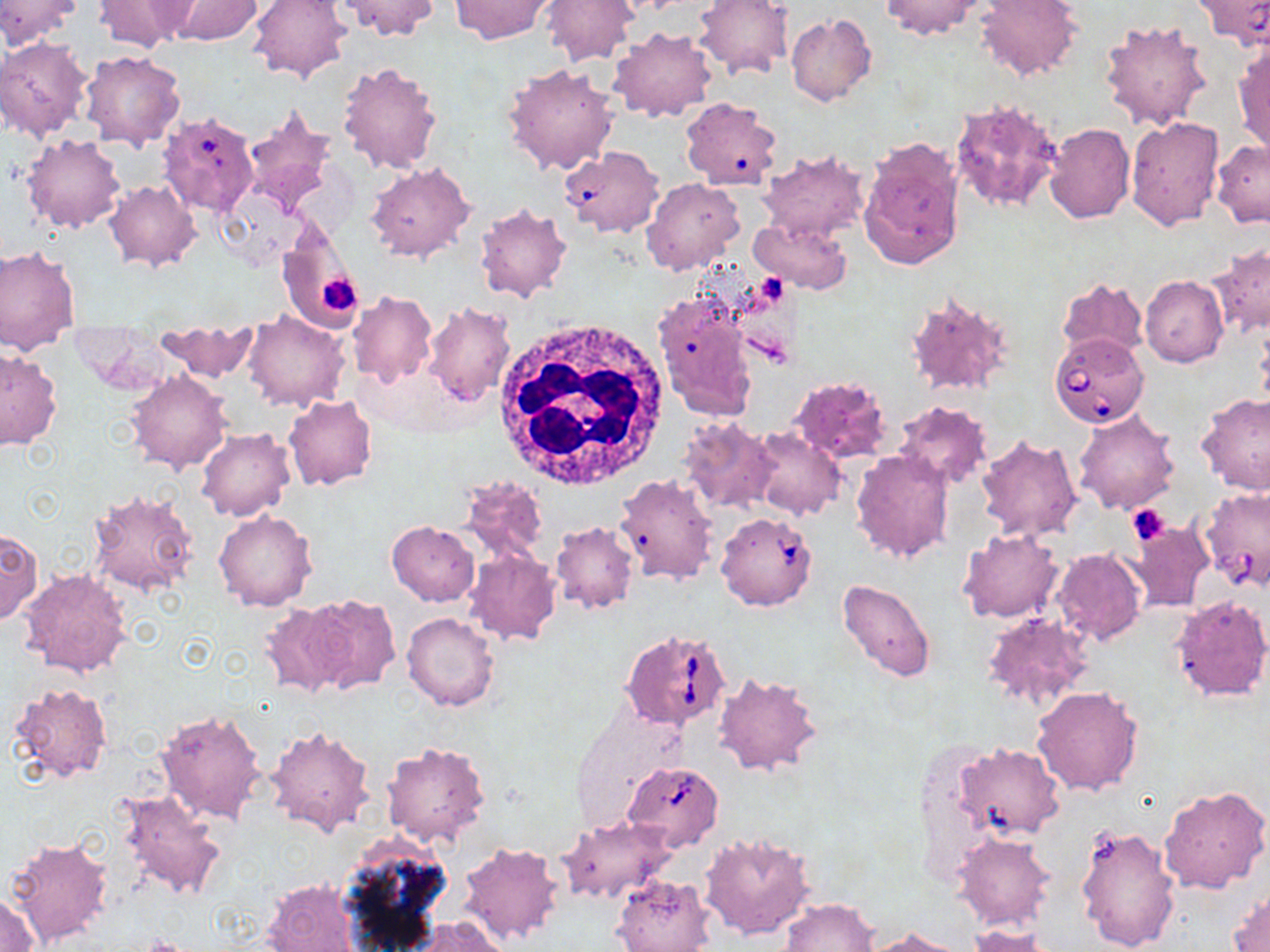
slide-level diagnosis = Babesia divergens
magnification = 1000x
uninfected red blood cell locations = approximate bounding boxes as (x1,y1)-(x2,y2) corner pairs in pixels: (0,0)-(83,48), (92,0)-(197,52), (162,0)-(263,44), (246,0)-(350,83), (334,0)-(440,41), (542,0)-(638,65), (693,0)-(793,79), (879,0)-(985,40), (975,0)-(1081,82), (449,1)-(555,43), (786,14)-(876,106), (1100,18)-(1211,131), (609,27)-(715,123), (0,38)-(91,140), (1233,40)-(1270,157), (81,50)-(186,150), (338,60)-(443,174), (502,63)-(621,175), (949,96)-(1066,213), (681,101)-(782,189), (239,104)-(339,217), (1126,117)-(1225,231), (1044,122)-(1135,223), (20,134)-(124,234), (858,139)-(965,271), (1210,140)-(1270,226), (560,148)-(659,236), (758,148)-(870,242), (366,162)-(475,264), (642,178)-(744,275), (105,181)-(201,271), (473,203)-(572,303), (748,217)-(852,295), (277,226)-(365,333), (1209,243)-(1269,336), (0,246)-(81,345), (1140,275)-(1228,369), (1056,277)-(1149,360), (653,286)-(760,420), (906,290)-(1015,398), (348,291)-(436,389), (423,303)-(515,407), (242,310)-(348,412), (156,324)-(257,384), (0,349)-(62,450), (125,370)-(231,474), (790,374)-(891,463), (1195,392)-(1270,494), (283,396)-(377,490), (893,401)-(993,489), (1073,409)-(1180,514), (676,417)-(780,512), (751,427)-(845,520), (196,428)-(293,521), (976,434)-(1081,541), (851,449)-(955,564), (614,474)-(719,585), (456,476)-(551,568), (87,489)-(199,596), (214,510)-(317,612), (1123,520)-(1213,614), (386,521)-(480,606), (550,521)-(638,614), (0,528)-(41,623), (957,529)-(1064,623), (464,550)-(561,646), (1052,550)-(1145,646), (19,569)-(131,679), (837,578)-(935,683), (299,593)-(401,693), (1170,593)-(1270,702), (259,604)-(350,699), (402,612)-(500,710), (982,612)-(1095,710), (713,672)-(823,777), (9,683)-(113,784), (1032,686)-(1144,796), (154,709)-(269,825), (265,726)-(376,838), (381,741)-(490,848), (953,748)-(1062,840), (1160,784)-(1270,893), (116,788)-(228,903), (557,817)-(675,905), (1074,823)-(1181,952), (698,831)-(817,940), (953,833)-(1057,930), (4,837)-(113,949), (334,837)-(454,952), (459,842)-(567,946), (612,874)-(713,952), (264,878)-(363,951), (1227,887)-(1270,951), (1,890)-(42,952), (779,897)-(880,951), (409,917)-(509,952), (967,925)-(1056,951), (862,926)-(972,952)
modality = light microscopy
image size = 1270×952 pixels
stain = May-Grünwald-Giemsa
preparation = thin blood film
field of view = single
Babesia divergens-infected red blood cell locations = approximate bounding boxes as (x1,y1)-(x2,y2) corner pairs in pixels: (154,115)-(257,220), (1050,333)-(1149,429), (1199,488)-(1270,592), (716,510)-(819,611), (622,629)-(728,733), (624,762)-(723,850)
platelet locations = approximate bounding boxes as (x1,y1)-(x2,y2) corner pairs in pixels: (313,273)-(361,320), (1127,503)-(1170,544)
white blood cell locations = approximate bounding boxes as (x1,y1)-(x2,y2) corner pairs in pixels: (493,321)-(671,490)